Draw a bounding box around every parasitised red blood cell, every trophozoite, every gametocyte, every leukocyte, and every artifact (platelet-like body, stain precipitate, or debris).
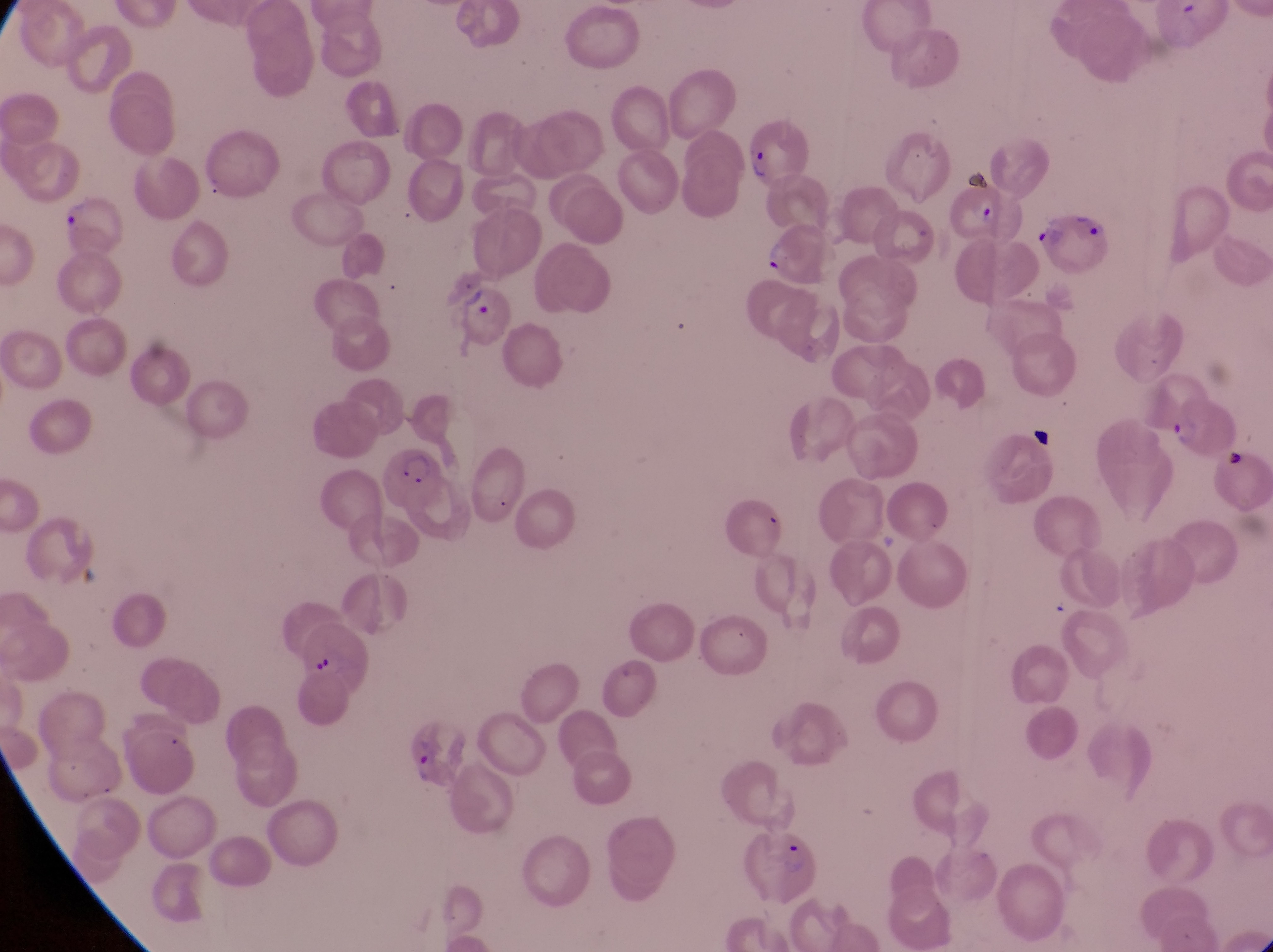

Approximate bounding boxes as {left, top, right, bottom} in pixels.
Parasitised red blood cells: {744, 113, 813, 187}, {953, 172, 1008, 240}, {1038, 195, 1113, 273}, {60, 197, 127, 259}, {442, 285, 509, 345}, {1166, 390, 1238, 460}, {382, 444, 437, 512}.
Trophozoites: {759, 225, 789, 273}, {405, 739, 442, 789}.
No leukocytes observed.
Artifacts (platelet-like body, stain precipitate, or debris): {302, 639, 335, 681}.

Magnification of 1000x. Photographed through the eyepiece of an Olympus CX-23 microscope with a smartphone camera. Collected in Uganda. Single field of view. Image is 1273×952 pixels. Thin blood smear.